Report the malaria status of this cell.
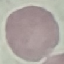

Uninfected.

Summary:
  - Preparation: thin blood smear
  - Image type: cell patch, automatically extracted from a larger field of view and resized to 64 × 64 pixels
  - Capture: smartphone through the microscope eyepiece
  - Stain: Giemsa